State the preparation type.
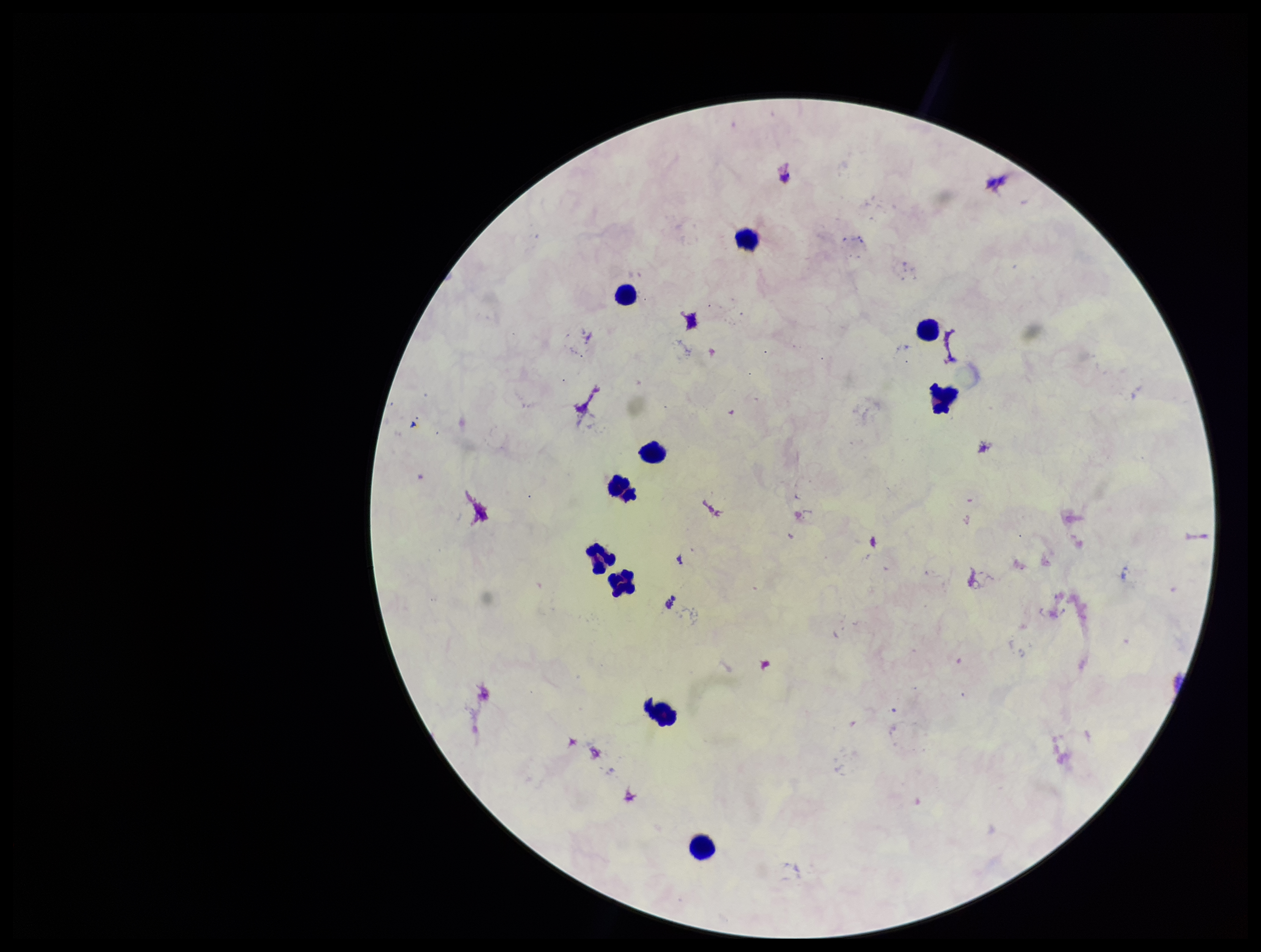

It is a thick blood smear.

field_of_view: single
patient_malaria_status: negative
plasmodium_parasites: none seen
capture: smartphone photograph through the microscope eyepiece
image_size: 1261×952 pixels
leukocyte_count: 10
parasite_count: 0
stain: Giemsa